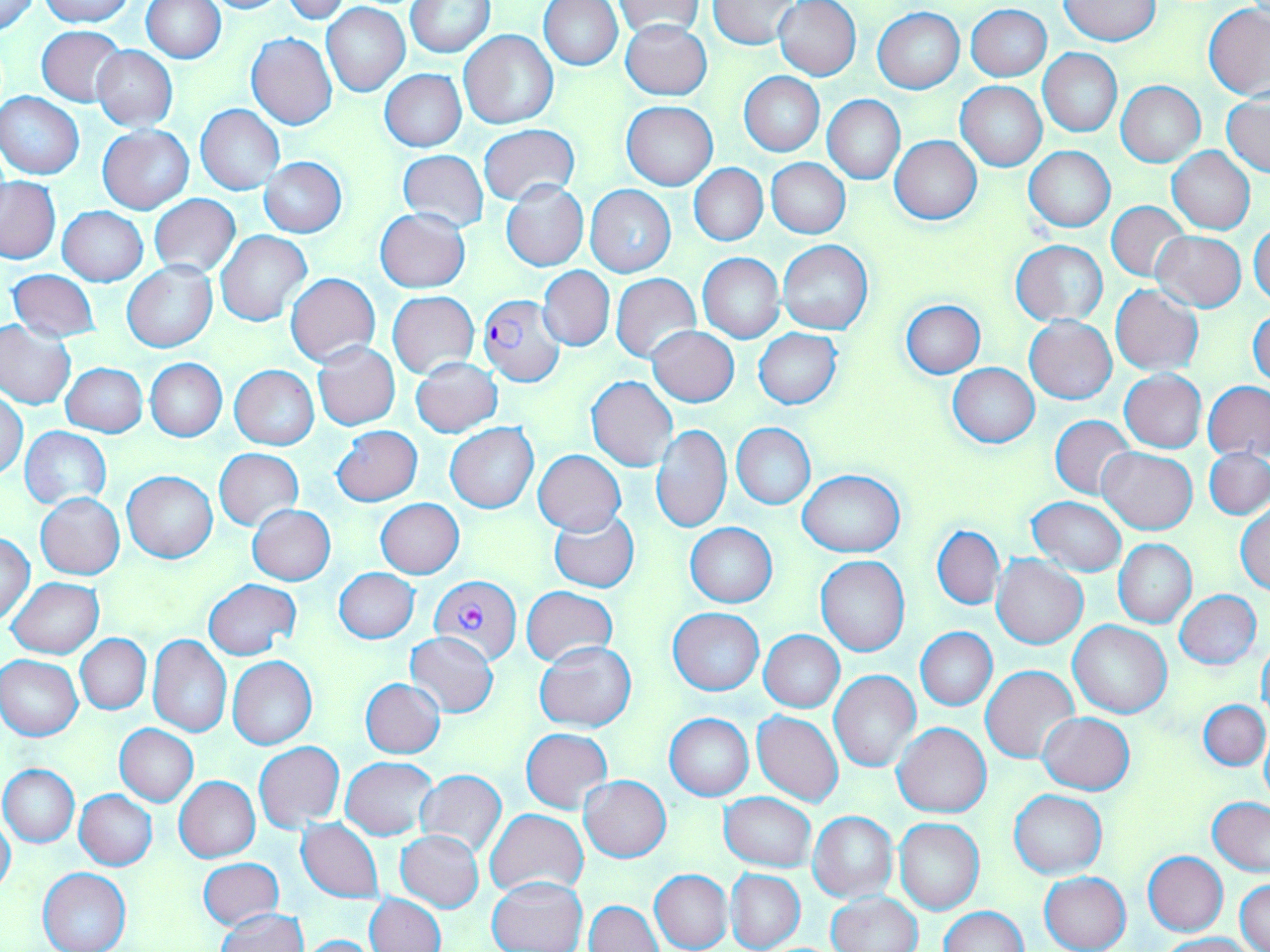 Approximate bounding boxes as (x1,y1)-(x2,y2) corner pairs in pixels. Uninfected red blood cell locations: (0,0)-(40,36), (38,0)-(136,26), (195,0)-(292,13), (709,0)-(798,49), (773,0)-(862,80), (141,1)-(225,63), (279,1)-(356,23), (407,1)-(493,56), (538,1)-(622,69), (1059,1)-(1159,45), (322,2)-(410,96), (614,2)-(705,38), (1202,3)-(1270,99), (967,5)-(1051,81), (873,8)-(964,93), (620,21)-(712,99), (36,25)-(125,104), (459,30)-(557,129), (246,33)-(337,131), (93,46)-(177,131), (1039,48)-(1121,137), (380,69)-(466,152), (740,71)-(824,156), (1117,80)-(1206,167), (956,82)-(1047,171), (0,91)-(84,179), (1224,94)-(1270,176), (823,95)-(905,184), (622,101)-(717,189), (196,104)-(285,194), (478,123)-(580,205), (99,126)-(193,214), (890,136)-(982,224), (1023,146)-(1114,231), (1167,148)-(1255,234), (398,150)-(488,231), (258,156)-(347,237), (767,159)-(850,239), (689,165)-(767,246), (1,178)-(60,262), (500,181)-(588,271), (585,186)-(676,277), (150,194)-(240,278), (1105,202)-(1191,281), (59,207)-(147,285), (375,209)-(469,292), (1249,222)-(1270,307), (216,230)-(310,325), (1151,231)-(1247,310), (778,240)-(873,335), (1010,240)-(1108,324), (698,253)-(784,343), (122,261)-(217,352), (538,266)-(614,351), (7,268)-(100,343), (286,273)-(380,365), (611,274)-(701,363), (1111,285)-(1203,375), (387,291)-(479,377), (899,299)-(984,378), (1249,308)-(1270,389), (1025,315)-(1116,405), (0,319)-(76,409), (648,327)-(739,406), (755,328)-(842,409), (312,341)-(400,430), (410,356)-(503,437), (145,358)-(226,441), (62,363)-(147,438), (948,364)-(1038,447), (230,365)-(319,450), (1120,371)-(1206,452), (586,376)-(678,472), (1203,381)-(1270,461), (1,390)-(27,480), (1051,415)-(1136,499), (445,423)-(539,513), (732,424)-(814,509), (331,425)-(422,505), (651,425)-(731,533), (21,426)-(111,510), (1098,447)-(1196,534), (1205,448)-(1270,519), (214,449)-(303,530), (532,450)-(626,536), (798,469)-(906,557), (123,470)-(217,562), (37,493)-(125,579), (1027,497)-(1126,577), (375,498)-(464,578), (1235,502)-(1270,595), (247,504)-(335,584), (548,510)-(639,593), (686,523)-(777,607), (933,526)-(1005,610), (2,532)-(35,624), (1113,539)-(1196,628), (992,555)-(1087,649), (816,557)-(909,657), (335,568)-(419,643), (7,578)-(103,659), (204,579)-(299,660), (522,586)-(618,667), (1175,591)-(1262,668), (668,608)-(763,695), (1069,621)-(1172,720), (915,628)-(996,711), (406,630)-(498,718), (759,630)-(844,713), (76,634)-(151,713), (147,635)-(231,736), (534,640)-(635,732), (1257,642)-(1270,716), (1,654)-(82,741), (228,656)-(317,750), (982,665)-(1079,763), (830,671)-(921,772), (359,678)-(444,757), (1200,700)-(1268,769), (753,712)-(843,806), (1038,712)-(1134,794), (664,714)-(753,800), (894,723)-(990,818), (114,724)-(197,806), (520,728)-(612,812), (1260,733)-(1270,808), (254,742)-(344,831), (342,757)-(436,840), (0,764)-(79,847), (416,768)-(506,858), (175,776)-(260,862), (580,776)-(671,862), (1010,789)-(1106,878), (74,790)-(157,869), (720,792)-(816,872), (1207,798)-(1270,874), (485,809)-(586,898), (808,811)-(897,900), (0,813)-(15,900), (297,819)-(384,903), (893,819)-(985,916), (396,830)-(484,912), (1144,852)-(1227,936), (199,858)-(284,930), (38,867)-(131,952), (649,869)-(732,952), (726,869)-(805,950), (1039,872)-(1130,952), (487,876)-(586,952), (1236,879)-(1270,952), (585,890)-(727,952), (828,891)-(922,952), (364,893)-(445,952), (586,900)-(662,951), (938,906)-(1028,952), (216,909)-(307,951), (1160,933)-(1256,951), (296,935)-(386,952). Plasmodium falciparum-infected red blood cell locations: (477,294)-(566,387), (430,576)-(522,662). Slide-level diagnosis: Plasmodium falciparum. Image is 1270×952 pixels. May-Grünwald-Giemsa stain. Thin blood film. One field of a larger specimen. Optical microscopy. Captured at 1000x magnification.